Locate and identify every blood parasite.
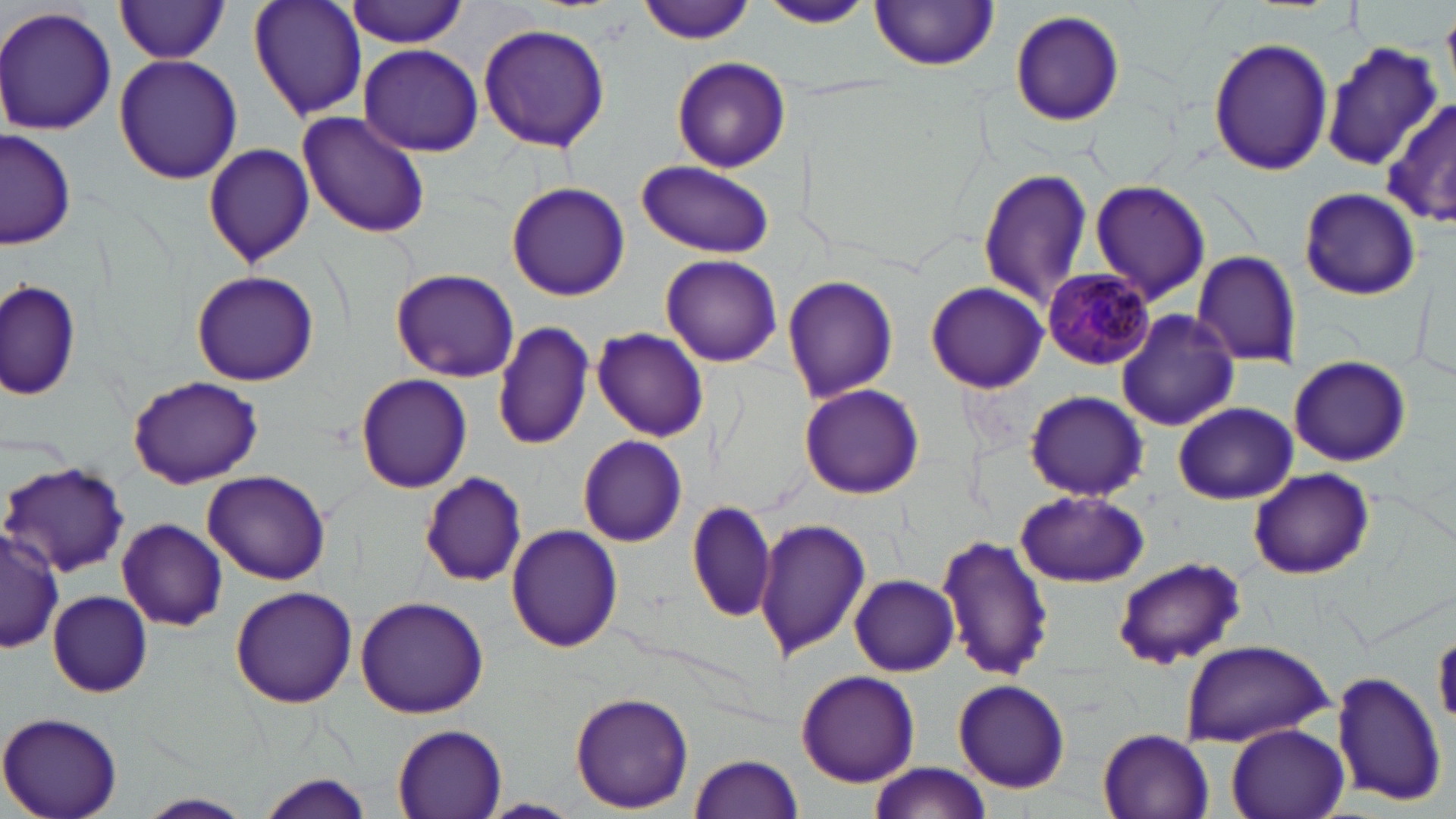
Approximate bounding boxes as (x1,y1)-(x2,y2) corner pairs in pixels.
Plasmodium malariae-infected red blood cells: (1041,268)-(1153,369).
No Plasmodium falciparum, Plasmodium ovale, Plasmodium vivax, Babesia divergens, or Trypanosoma brucei observed.

Uninfected red blood cell locations: (247,0)-(368,121), (347,0)-(472,47), (638,0)-(759,44), (760,0)-(871,29), (115,1)-(232,64), (872,1)-(999,72), (0,4)-(119,138), (1008,10)-(1126,127), (477,22)-(611,154), (1206,37)-(1331,175), (358,43)-(483,157), (1322,43)-(1441,170), (114,54)-(244,183), (670,57)-(791,173), (1380,102)-(1456,226), (299,109)-(431,240), (1,130)-(76,250), (204,141)-(316,267), (635,159)-(773,258), (976,167)-(1092,306), (1090,179)-(1210,306), (507,182)-(630,301), (1295,185)-(1422,300), (1191,252)-(1301,367), (660,253)-(783,366), (391,268)-(519,383), (190,269)-(319,387), (783,275)-(901,403), (2,278)-(80,400), (925,279)-(1048,393), (1115,310)-(1242,431), (493,321)-(593,450), (590,326)-(707,443), (1285,357)-(1415,468), (355,374)-(472,493), (127,376)-(265,489), (799,383)-(925,498), (1022,390)-(1148,501), (1173,403)-(1299,505), (577,435)-(689,546), (3,462)-(129,577), (1247,468)-(1374,580), (419,471)-(527,588), (202,472)-(331,583), (1013,489)-(1151,587), (687,499)-(780,627), (753,518)-(869,661), (117,519)-(226,631), (506,524)-(623,652), (0,526)-(63,655), (937,534)-(1056,681), (1112,556)-(1246,669), (849,574)-(959,675), (230,587)-(357,708), (47,591)-(152,698), (355,595)-(490,718), (1433,627)-(1456,728), (1177,640)-(1331,747), (1328,668)-(1446,807), (796,670)-(920,787), (952,679)-(1070,793), (569,691)-(694,813), (0,711)-(124,819), (391,722)-(509,817), (1224,723)-(1351,819), (1098,729)-(1214,819), (688,752)-(804,819), (867,762)-(990,819), (253,770)-(376,817), (136,793)-(254,819), (478,797)-(583,818). Slide-level diagnosis: Plasmodium malariae. Image is 1456×819 pixels. One field of a larger specimen. May-Grünwald-Giemsa stain. Captured at 1000x magnification. Optical microscopy. Thin blood smear.